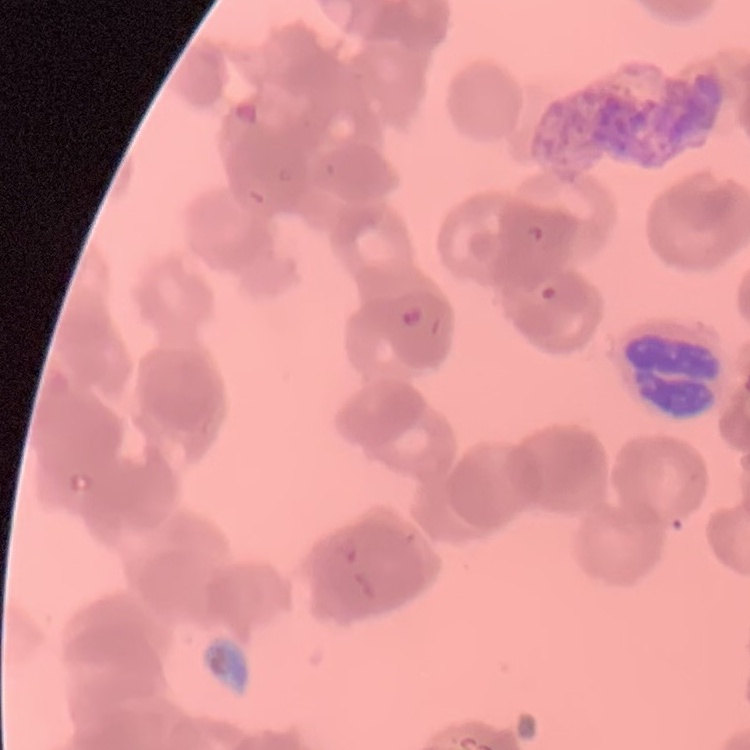
red blood cell morphology = rouleaux formation
image type = one tile cut from a larger photomicrograph
preparation = thin blood film
stain = Field's or Giemsa